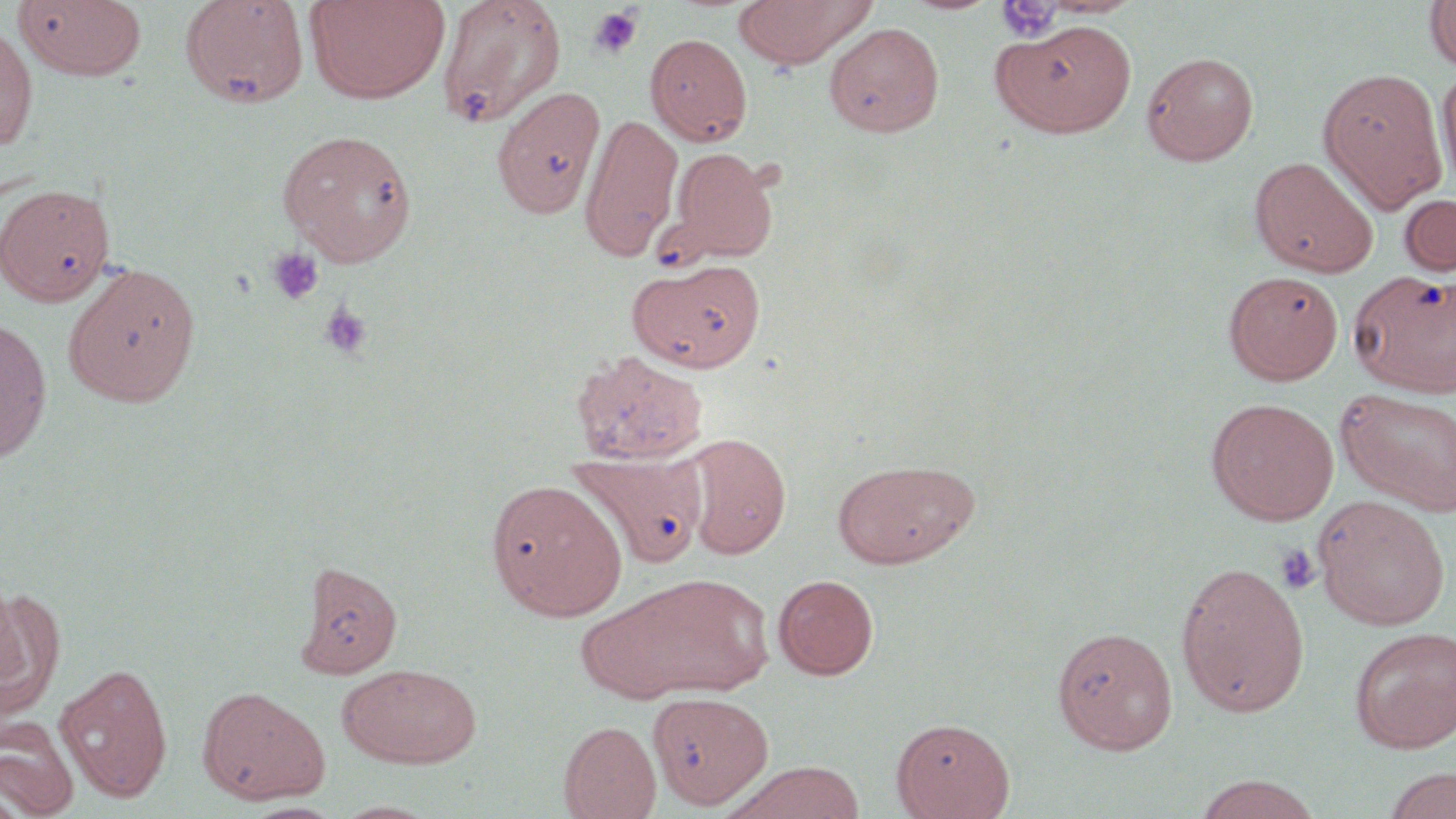
Summary:
  - Coordinate format: approximate bounding boxes as named x1/y1/x2/y2 corners in pixels
  - Uninfected red blood cell locations: (x1=179, y1=0, x2=310, y2=109), (x1=305, y1=0, x2=450, y2=103), (x1=437, y1=0, x2=567, y2=129), (x1=733, y1=0, x2=876, y2=68), (x1=897, y1=0, x2=1003, y2=15), (x1=1424, y1=0, x2=1456, y2=73), (x1=14, y1=1, x2=147, y2=81), (x1=996, y1=18, x2=1139, y2=137), (x1=0, y1=22, x2=38, y2=152), (x1=824, y1=22, x2=944, y2=138), (x1=645, y1=32, x2=753, y2=146), (x1=1141, y1=51, x2=1259, y2=165), (x1=1437, y1=63, x2=1456, y2=193), (x1=1317, y1=67, x2=1447, y2=211), (x1=491, y1=86, x2=605, y2=220), (x1=579, y1=113, x2=684, y2=261), (x1=277, y1=129, x2=418, y2=265), (x1=668, y1=147, x2=779, y2=264), (x1=1249, y1=156, x2=1379, y2=278), (x1=0, y1=179, x2=112, y2=309), (x1=1398, y1=193, x2=1456, y2=278), (x1=629, y1=259, x2=765, y2=372), (x1=63, y1=263, x2=202, y2=407), (x1=1349, y1=269, x2=1456, y2=397), (x1=1224, y1=270, x2=1343, y2=385), (x1=0, y1=317, x2=53, y2=464), (x1=570, y1=349, x2=709, y2=466), (x1=1337, y1=387, x2=1456, y2=516), (x1=1206, y1=397, x2=1339, y2=525), (x1=681, y1=433, x2=791, y2=559), (x1=569, y1=450, x2=706, y2=570), (x1=833, y1=458, x2=979, y2=569), (x1=485, y1=479, x2=627, y2=621), (x1=1313, y1=495, x2=1451, y2=630), (x1=295, y1=561, x2=402, y2=679), (x1=1174, y1=561, x2=1310, y2=717), (x1=597, y1=571, x2=777, y2=704), (x1=773, y1=574, x2=879, y2=679), (x1=0, y1=586, x2=65, y2=720), (x1=1052, y1=626, x2=1178, y2=753), (x1=1349, y1=626, x2=1456, y2=753), (x1=54, y1=662, x2=173, y2=803), (x1=338, y1=662, x2=483, y2=768), (x1=196, y1=685, x2=330, y2=805), (x1=649, y1=691, x2=774, y2=811), (x1=0, y1=717, x2=80, y2=819), (x1=891, y1=717, x2=1015, y2=819), (x1=558, y1=720, x2=661, y2=818), (x1=724, y1=761, x2=867, y2=819), (x1=1380, y1=767, x2=1456, y2=819), (x1=1191, y1=774, x2=1324, y2=819), (x1=0, y1=784, x2=26, y2=819), (x1=330, y1=800, x2=442, y2=818)
  - Platelet locations: (x1=996, y1=1, x2=1064, y2=42), (x1=588, y1=5, x2=644, y2=59), (x1=267, y1=247, x2=325, y2=305), (x1=318, y1=303, x2=373, y2=359), (x1=1275, y1=544, x2=1321, y2=595)
  - Slide-level diagnosis: negative for blood parasites
  - Stain: May-Grünwald-Giemsa
  - Magnification: 1000x
  - Field of view: single
  - Image size: 1456×819 pixels
  - Preparation: thin blood film
  - Modality: light microscopy